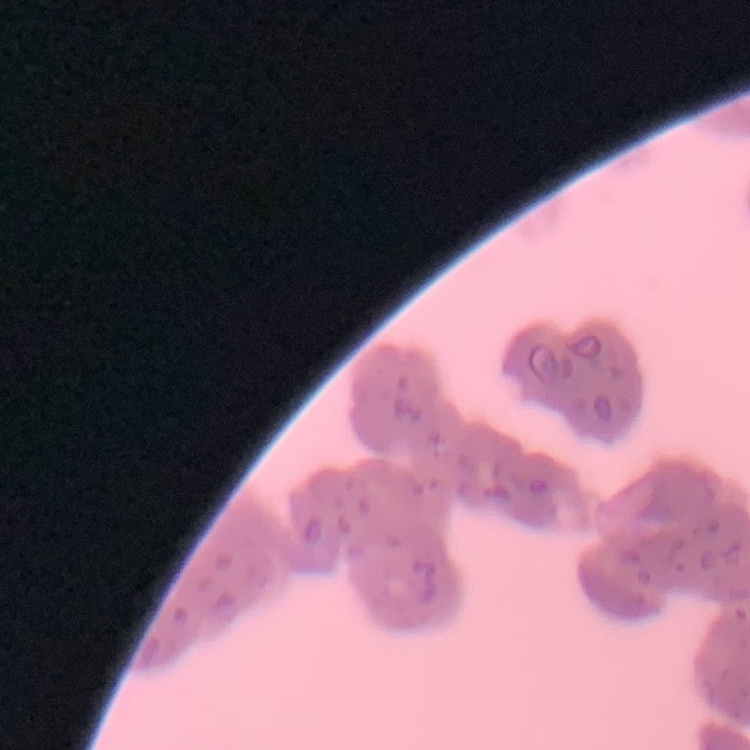
The erythrocytes exhibit rouleaux formation. Thin peripheral smear. Stained with either Field's or Giemsa. One tile cut from a larger photomicrograph.